Comment on the morphology of the red blood cells.
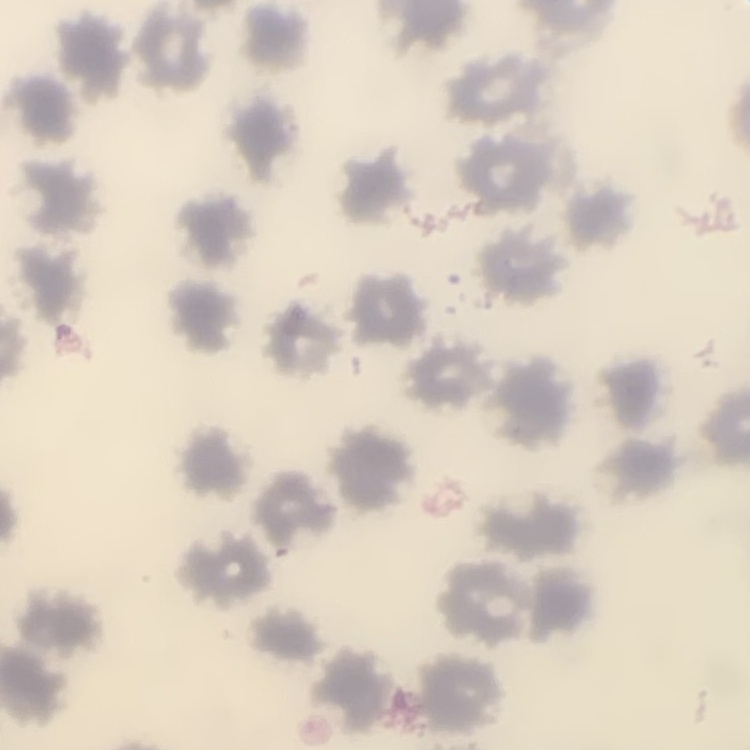

No rouleaux formation.

Summary:
  - Stain: Field's or Giemsa
  - Preparation: thin blood smear
  - Image type: one tile cut from a larger photomicrograph